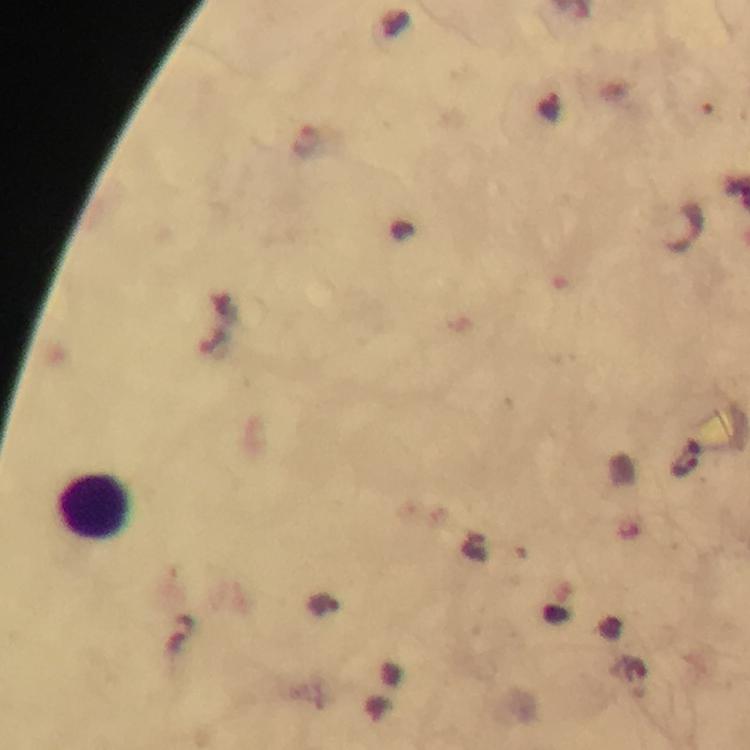
Approximate centers as {x, y} in pixels. Leukocyte locations: {93, 506}. Plasmodium parasite locations: {307, 142}. Immersion oil applied. Thick blood smear. Giemsa stain. 100x magnification. Smartphone photograph taken through a microscope. Image is 750×750 pixels. From a diagnostic examination for malaria. A crop from one field of view.